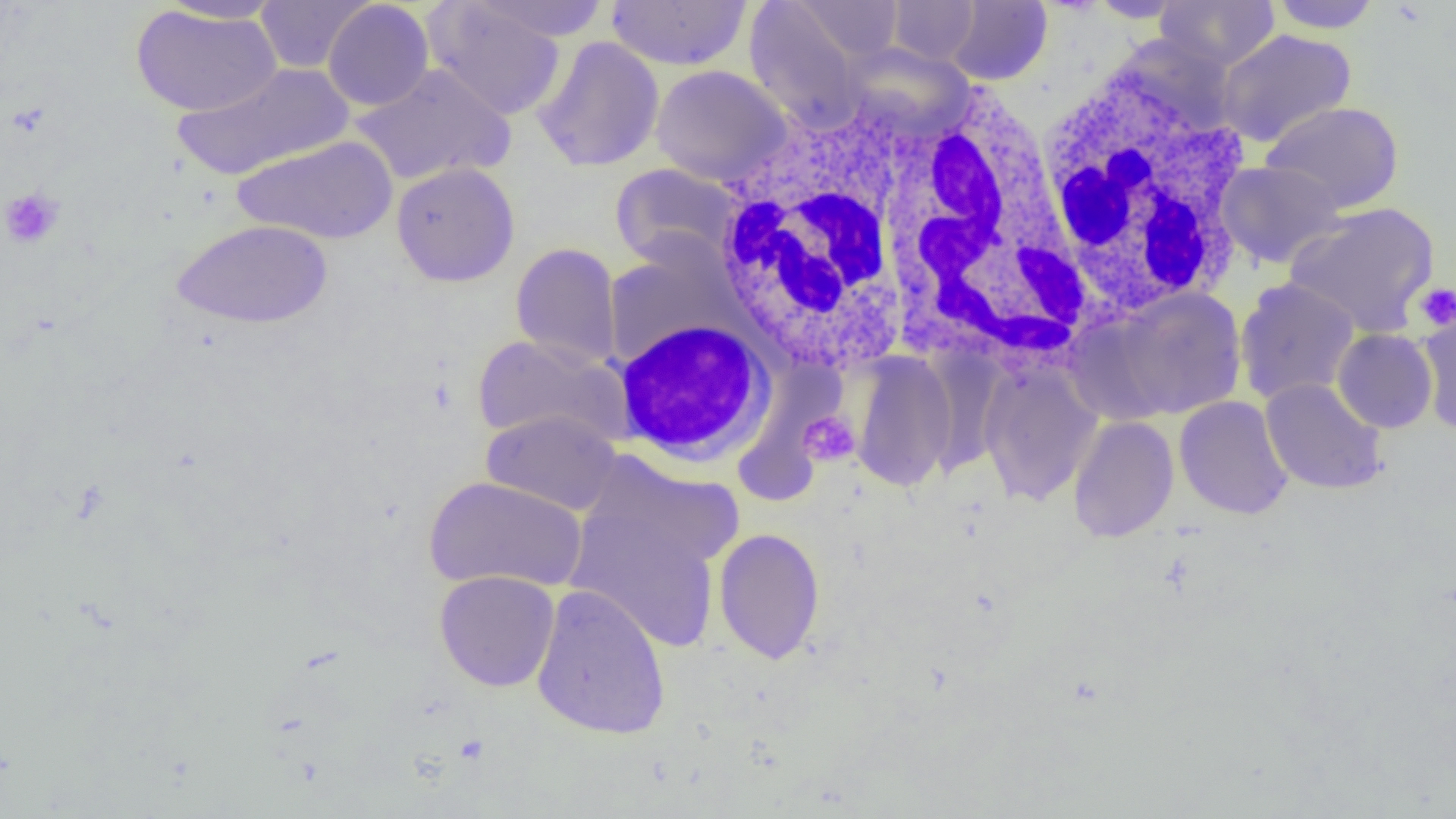
Approximate bounding boxes as (x1, y1, x2, y2) in pixels. White blood cell locations: (1029, 59, 1256, 319), (717, 73, 1082, 384), (612, 317, 777, 468). Uninfected red blood cell locations: (154, 0, 289, 24), (255, 0, 373, 74), (471, 0, 613, 41), (606, 0, 753, 70), (943, 0, 1052, 85), (1086, 0, 1190, 23), (1155, 0, 1280, 72), (1265, 0, 1384, 33), (322, 1, 434, 111), (424, 1, 566, 121), (744, 1, 866, 129), (790, 1, 905, 64), (887, 1, 982, 65), (130, 5, 282, 116), (1216, 29, 1357, 147), (532, 36, 665, 173), (842, 43, 972, 138), (172, 63, 353, 181), (351, 63, 515, 187), (650, 65, 791, 185), (1261, 101, 1404, 214), (232, 135, 398, 245), (1217, 160, 1347, 268), (391, 162, 520, 287), (610, 163, 742, 269), (1283, 202, 1440, 338), (171, 219, 332, 330), (510, 242, 623, 369), (1234, 277, 1361, 405), (1106, 287, 1248, 420), (1417, 311, 1456, 435), (1332, 328, 1437, 433), (473, 334, 631, 448), (850, 352, 957, 492), (978, 364, 1101, 506), (1260, 378, 1388, 495), (1174, 396, 1293, 520), (481, 410, 623, 516), (1067, 415, 1179, 542), (579, 453, 745, 576), (425, 475, 588, 593), (566, 507, 720, 654), (714, 527, 825, 664), (434, 570, 560, 692), (531, 583, 672, 740). Platelet locations: (0, 187, 64, 249), (1415, 283, 1456, 331), (798, 411, 860, 466). Slide-level diagnosis: negative for blood parasites. One field of a larger specimen. 1000x magnification. Image is 1456×819 pixels. Thin blood film. Light microscopy.